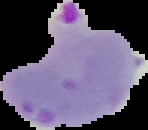

image_size: 148×130 pixels
preparation: thin blood smear
result: Plasmodium parasites identified
image_type: segmented cell region on a black background